Classify this cell by malaria status.
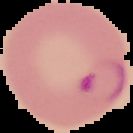
It is parasitized.

Summary:
  - Image type: segmented cell region on a black background
  - Image size: 133×133 pixels
  - Preparation: thin blood film